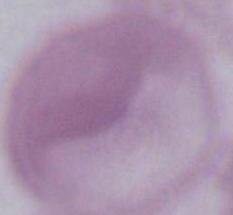

magnification = 1000x
modality = micrograph
identification = red blood cell